Locate and identify every blood parasite.
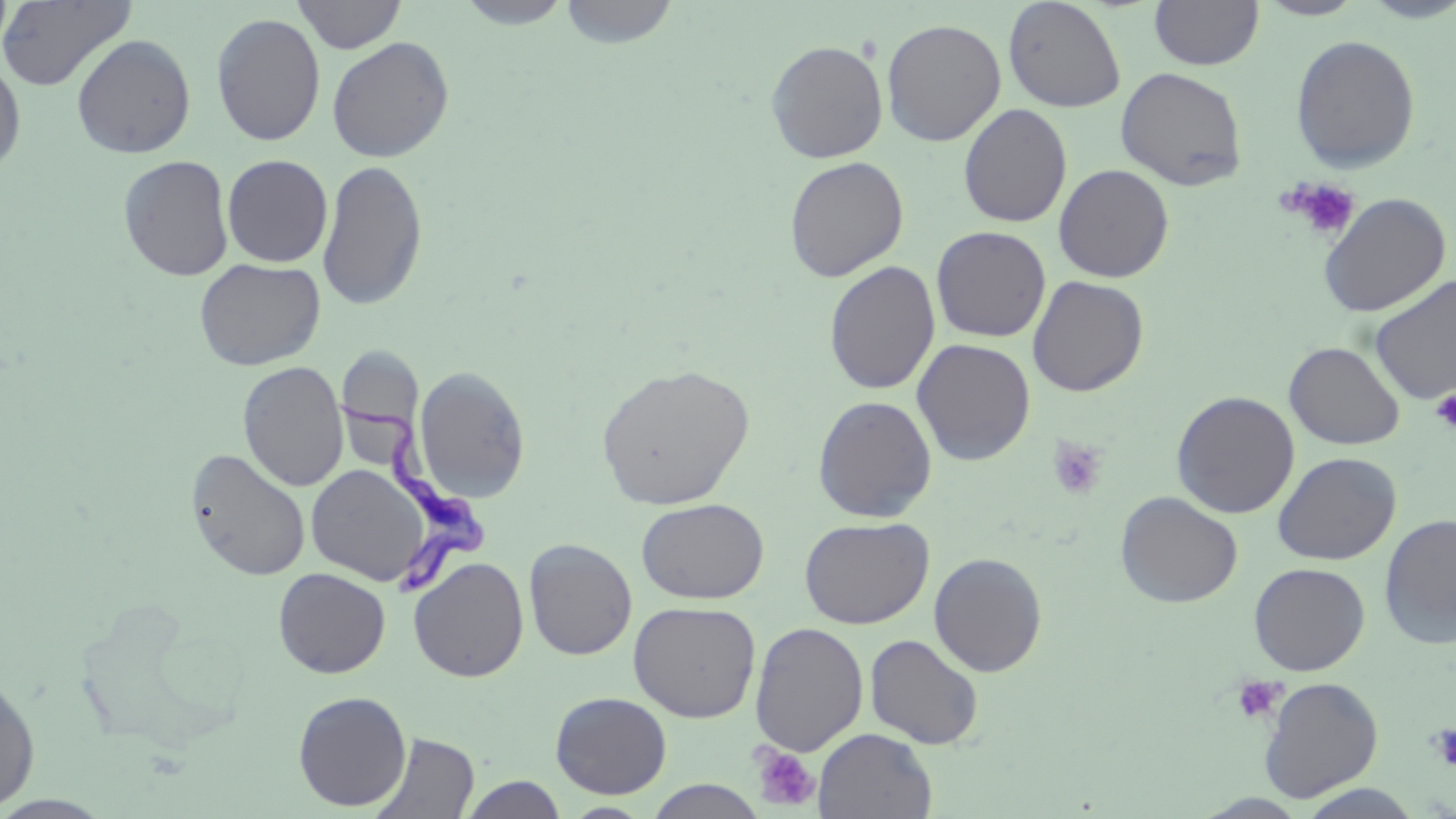

Approximate bounding boxes as named x1/y1/x2/y2 corners in pixels.
Trypanosoma brucei: (x1=331, y1=388, x2=498, y2=596).
No Plasmodium falciparum, Plasmodium ovale, Plasmodium malariae, Plasmodium vivax, or Babesia divergens observed.

Uninfected red blood cell locations: (x1=0, y1=0, x2=138, y2=92), (x1=292, y1=0, x2=407, y2=53), (x1=453, y1=0, x2=576, y2=29), (x1=557, y1=0, x2=680, y2=49), (x1=1002, y1=0, x2=1126, y2=112), (x1=1148, y1=0, x2=1265, y2=70), (x1=1355, y1=0, x2=1456, y2=23), (x1=1256, y1=1, x2=1367, y2=20), (x1=211, y1=13, x2=325, y2=146), (x1=881, y1=18, x2=1006, y2=147), (x1=71, y1=34, x2=196, y2=159), (x1=1290, y1=34, x2=1421, y2=173), (x1=326, y1=36, x2=454, y2=163), (x1=765, y1=40, x2=888, y2=163), (x1=0, y1=54, x2=26, y2=177), (x1=1115, y1=67, x2=1248, y2=191), (x1=958, y1=103, x2=1072, y2=228), (x1=118, y1=154, x2=235, y2=281), (x1=222, y1=154, x2=333, y2=267), (x1=784, y1=156, x2=908, y2=282), (x1=317, y1=158, x2=428, y2=312), (x1=1053, y1=163, x2=1174, y2=283), (x1=1318, y1=193, x2=1451, y2=317), (x1=931, y1=226, x2=1052, y2=342), (x1=193, y1=257, x2=326, y2=372), (x1=823, y1=261, x2=941, y2=395), (x1=1368, y1=273, x2=1456, y2=405), (x1=1027, y1=275, x2=1149, y2=397), (x1=912, y1=338, x2=1035, y2=466), (x1=1284, y1=341, x2=1405, y2=450), (x1=238, y1=361, x2=348, y2=492), (x1=596, y1=363, x2=755, y2=510), (x1=413, y1=365, x2=530, y2=502), (x1=1171, y1=391, x2=1300, y2=519), (x1=812, y1=395, x2=938, y2=522), (x1=185, y1=447, x2=311, y2=581), (x1=1272, y1=451, x2=1401, y2=565), (x1=306, y1=462, x2=433, y2=586), (x1=1114, y1=491, x2=1242, y2=608), (x1=637, y1=498, x2=769, y2=604), (x1=1379, y1=514, x2=1456, y2=650), (x1=799, y1=516, x2=934, y2=629), (x1=523, y1=538, x2=637, y2=660), (x1=929, y1=552, x2=1047, y2=677), (x1=408, y1=556, x2=529, y2=683), (x1=1248, y1=562, x2=1370, y2=676), (x1=273, y1=567, x2=391, y2=679), (x1=628, y1=600, x2=761, y2=722), (x1=750, y1=621, x2=869, y2=756), (x1=865, y1=633, x2=984, y2=749), (x1=0, y1=672, x2=40, y2=812), (x1=1258, y1=676, x2=1383, y2=802), (x1=293, y1=690, x2=412, y2=811), (x1=551, y1=692, x2=672, y2=799), (x1=814, y1=728, x2=937, y2=819), (x1=369, y1=732, x2=479, y2=818), (x1=459, y1=775, x2=567, y2=818), (x1=642, y1=779, x2=768, y2=818), (x1=1294, y1=784, x2=1427, y2=818), (x1=561, y1=802, x2=654, y2=817). Platelet locations: (x1=1282, y1=178, x2=1361, y2=242), (x1=1430, y1=389, x2=1456, y2=432), (x1=1047, y1=437, x2=1109, y2=500), (x1=1231, y1=676, x2=1284, y2=724), (x1=1426, y1=722, x2=1456, y2=772), (x1=750, y1=744, x2=820, y2=812). Slide-level diagnosis: Trypanosoma brucei. Thin blood smear. Image is 1456×819 pixels. May-Grünwald-Giemsa-stained preparation. Light microscopy. Single field of view. Captured at 1000x magnification.